Point out every malaria parasite.
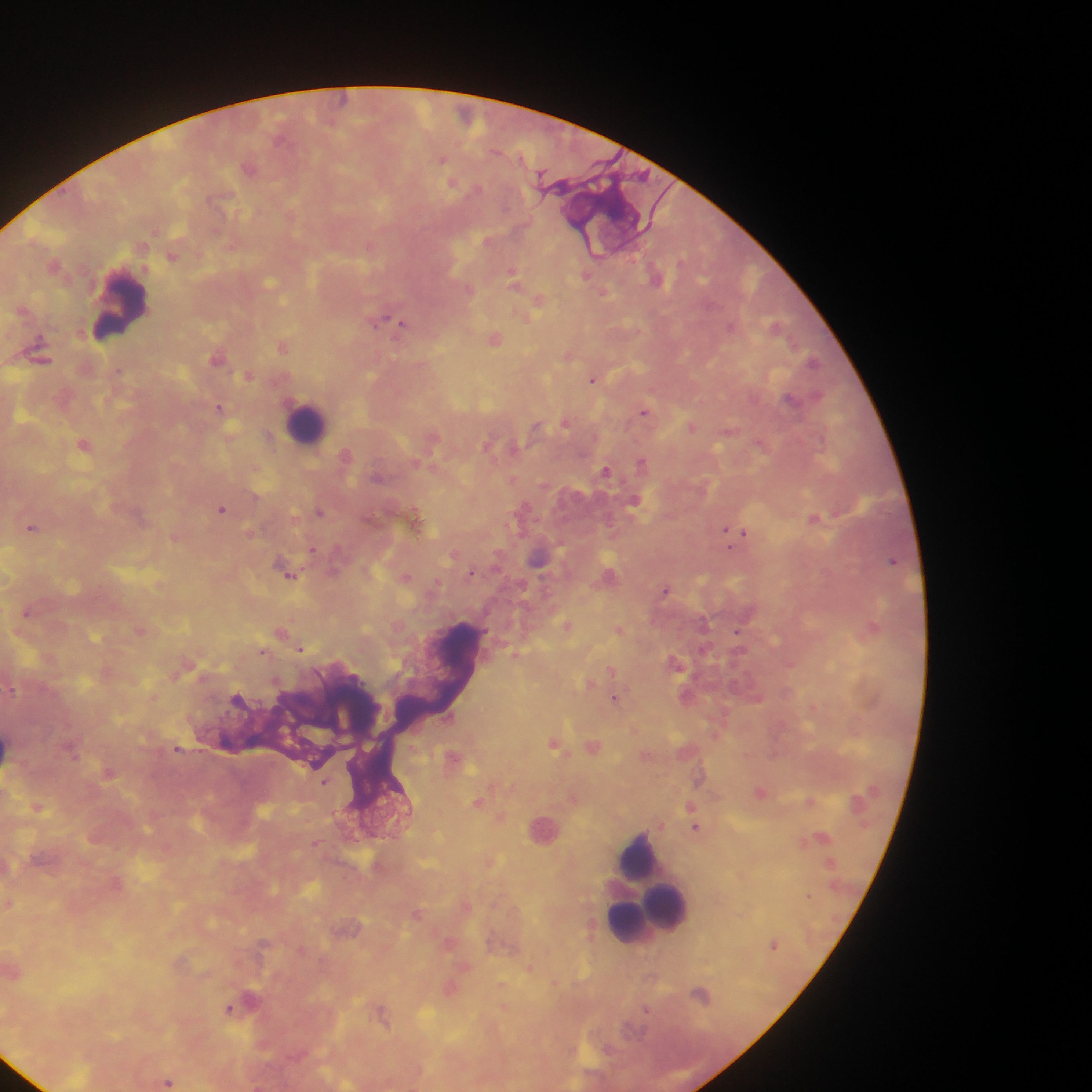
Approximate centers as x y in pixels.
Malaria parasites: 343 100; 280 138; 442 159; 249 168; 542 175; 452 183; 477 188; 172 256; 54 265; 512 273; 586 275; 655 278; 271 281; 604 293; 539 300; 380 321; 402 324; 730 327; 495 339; 283 347; 568 355; 217 357; 813 361; 248 376; 593 379; 790 399; 218 406; 644 412; 566 424; 691 428; 84 444; 346 454; 642 462; 605 470; 634 499; 222 509; 320 511; 415 516; 813 518; 32 527; 726 531; 743 533; 313 549; 892 560; 471 573; 290 576; 666 590; 27 612; 703 623; 567 625; 873 627; 140 630; 620 630; 282 631; 737 631; 301 648; 263 652; 515 653; 611 670; 12 690; 237 697; 614 698; 449 716; 553 743; 178 749; 71 751; 325 782; 477 802; 501 817; 695 827; 315 843; 417 913; 529 967; 228 1008; 646 1010; 168 1082.

leukocyte locations = approximate centers as x y in pixels: 121 309; 307 423; 10 748; 640 860; 649 885; 661 902
field of view = single
preparation = thick blood film
capture = mobile-phone photograph through a microscope
image size = 1092×1092 pixels
country = Ghana